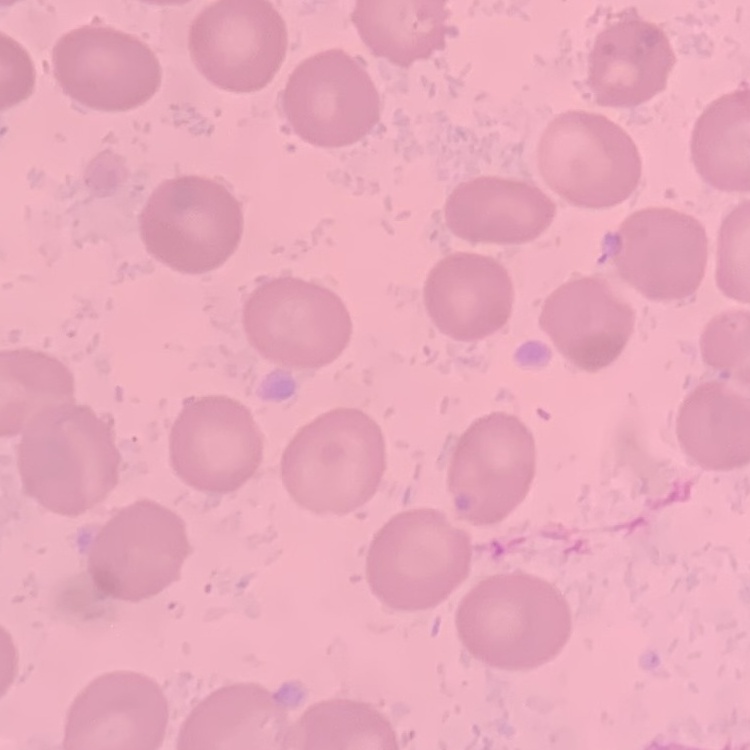

Summary:
  - Red blood cell morphology: no rouleaux formation
  - Preparation: thin peripheral smear
  - Stain: Field's or Giemsa
  - Image type: one tile cut from a larger photomicrograph